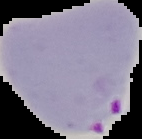
image type = segmented cell region with the area outside set to black
result = Plasmodium parasites identified
image size = 142×139 pixels
preparation = thin blood smear